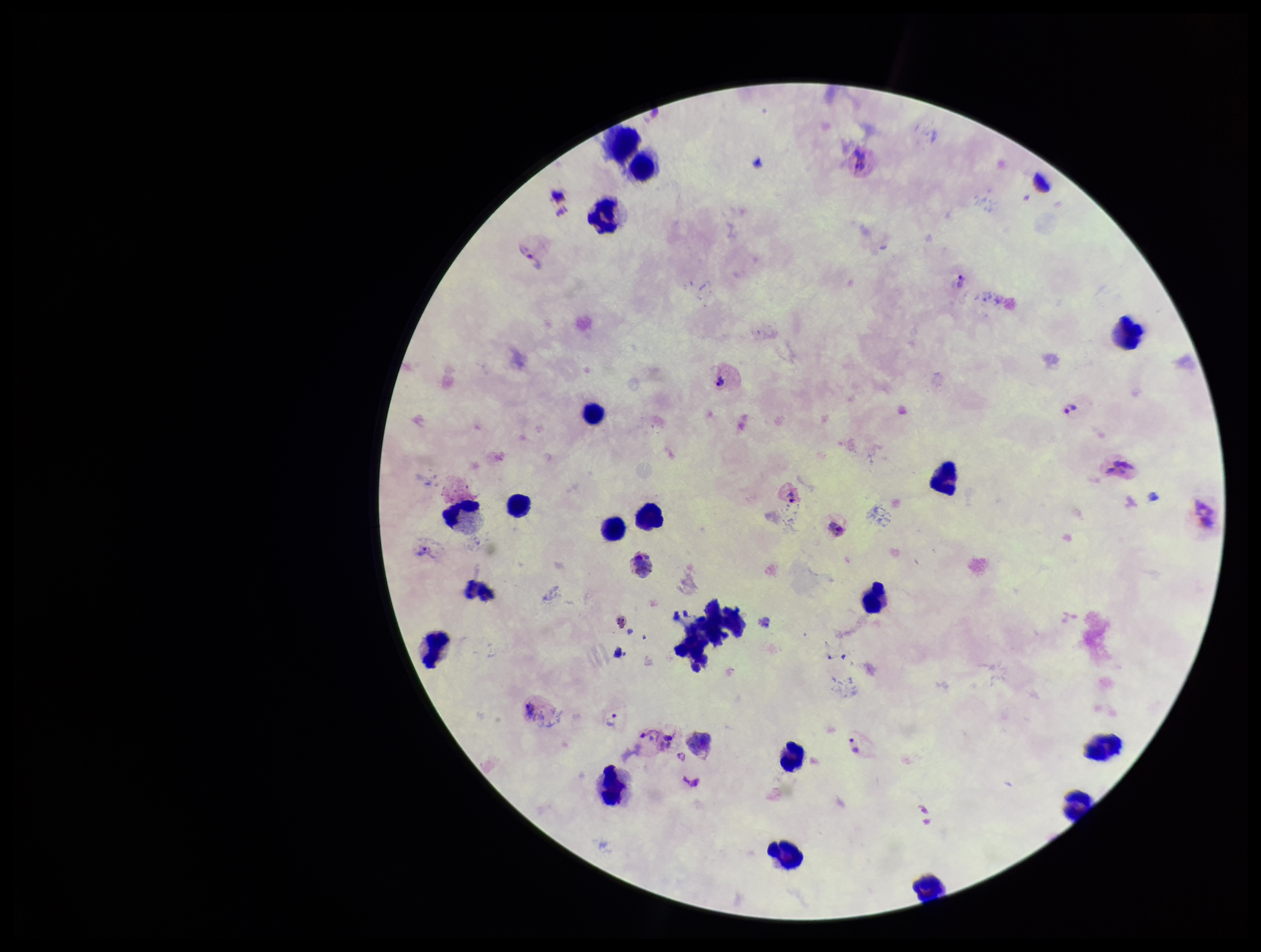
leukocyte count = 22
image size = 1261×952 pixels
parasite count = 8
capture = smartphone photograph through the microscope eyepiece
preparation = thick
Plasmodium parasites = seen
species reported for this patient = Plasmodium vivax
patient malaria status = positive
stain = Giemsa
field of view = single